Describe the morphology of the erythrocytes.
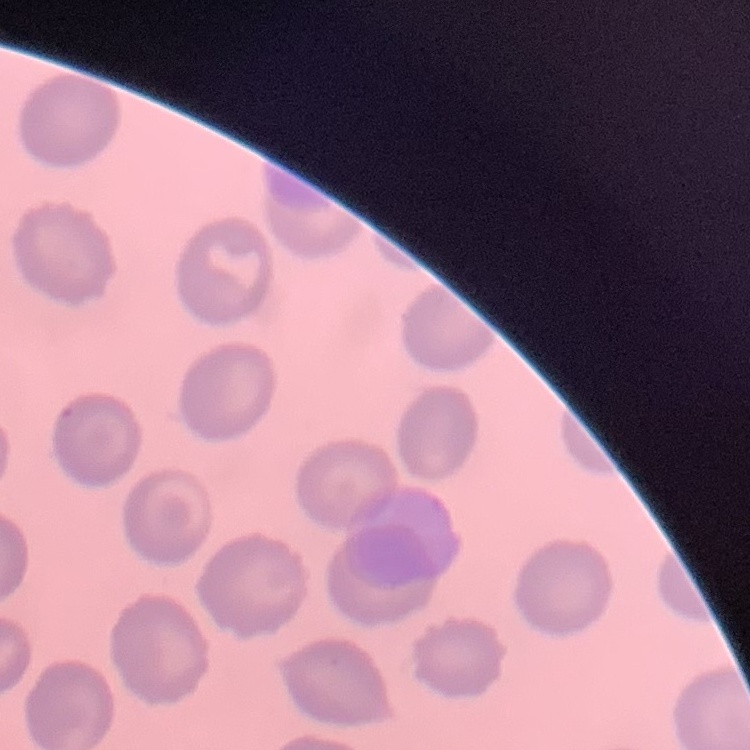
No rouleaux formation.

Summary:
  - Image type: one tile cut from a larger photomicrograph
  - Preparation: thin peripheral smear
  - Stain: Field's or Giemsa